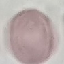
Summary:
  - Result: negative for malaria parasites
  - Stain: Giemsa
  - Capture: smartphone through the microscope eyepiece
  - Image type: cell patch, automatically extracted from a larger field of view and resized to 64 × 64 pixels
  - Preparation: thin smear